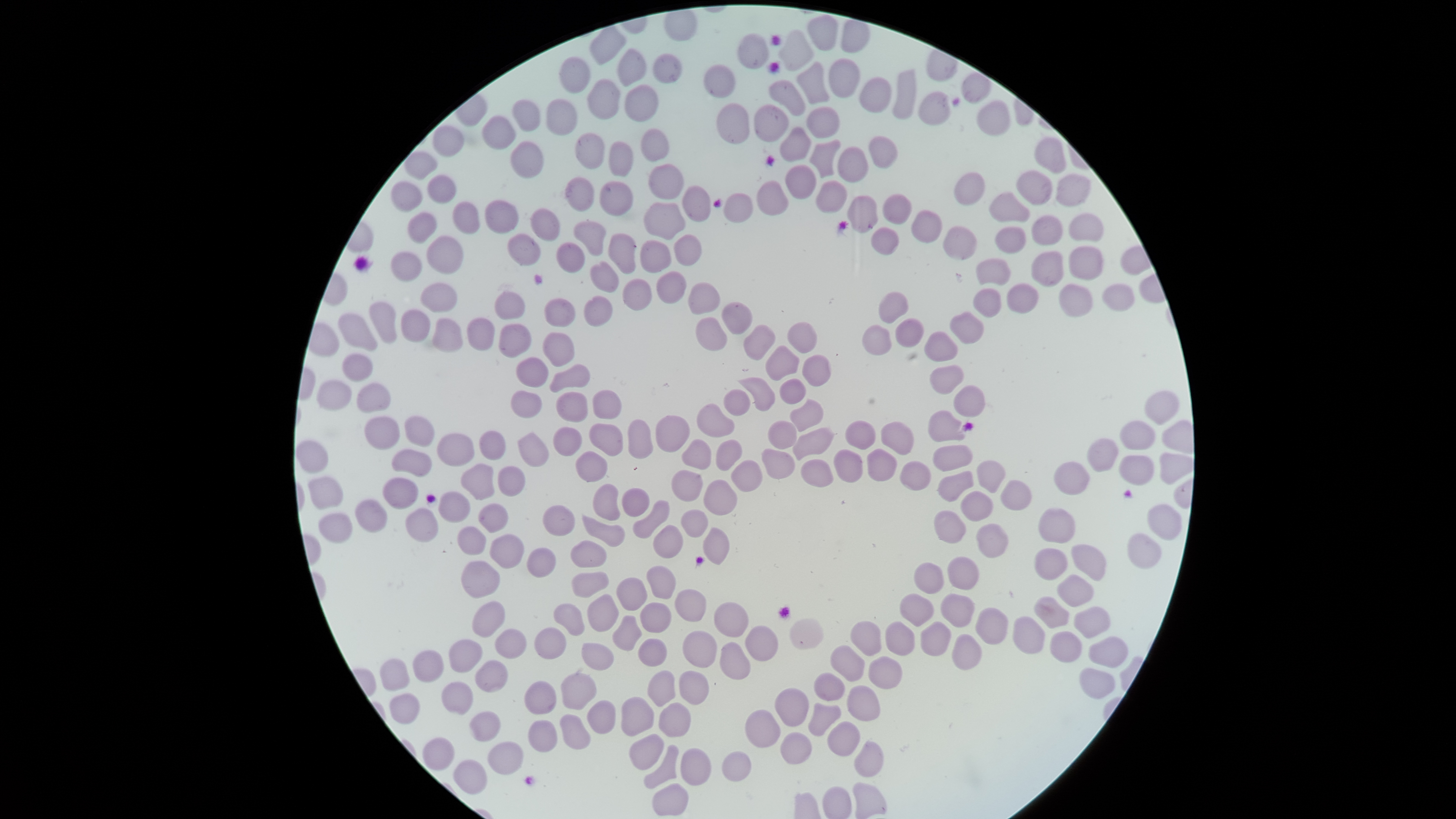
Approximate bounding boxes as (left, top, right, bottom) in pixels.
Summary:
  - Uninfected red blood cells: (807, 14, 839, 51), (842, 20, 871, 54), (589, 27, 628, 66), (777, 29, 813, 71), (738, 32, 769, 69), (618, 49, 646, 87), (651, 54, 682, 84), (560, 57, 591, 94), (828, 59, 860, 98), (799, 62, 829, 104), (704, 65, 734, 98), (893, 69, 917, 119), (859, 77, 892, 113), (770, 79, 804, 116), (588, 80, 620, 121), (625, 85, 659, 122), (919, 91, 952, 125), (512, 100, 541, 132), (545, 100, 576, 136), (978, 100, 1011, 136), (716, 104, 749, 143), (754, 104, 789, 142), (807, 106, 840, 138), (482, 116, 515, 150), (432, 126, 465, 158), (780, 127, 812, 162), (640, 128, 669, 161), (573, 133, 604, 170), (869, 135, 898, 168), (1034, 137, 1066, 173), (810, 140, 841, 178), (510, 142, 543, 178), (609, 142, 634, 178), (837, 146, 869, 182), (404, 152, 438, 179), (648, 164, 684, 200), (785, 165, 817, 199), (1015, 170, 1052, 205), (954, 173, 985, 205), (1056, 174, 1090, 206), (427, 176, 456, 204), (565, 178, 594, 212), (390, 181, 422, 213), (599, 181, 633, 216), (816, 181, 848, 213), (757, 182, 789, 215), (681, 186, 711, 222), (722, 193, 753, 223), (883, 193, 912, 224), (990, 193, 1031, 222), (485, 200, 520, 234), (452, 201, 481, 234), (643, 202, 686, 241), (529, 209, 561, 243), (911, 210, 943, 243), (406, 212, 439, 244), (1068, 213, 1104, 241), (1032, 215, 1062, 246), (573, 221, 606, 256), (942, 226, 976, 260), (996, 226, 1026, 252), (871, 227, 899, 256), (507, 233, 541, 266), (608, 234, 635, 274), (674, 235, 701, 267), (426, 236, 464, 274), (640, 240, 672, 274), (556, 242, 586, 273), (1068, 247, 1102, 280), (390, 252, 422, 282), (1031, 252, 1065, 287), (976, 258, 1012, 284), (590, 261, 619, 294), (657, 271, 687, 305), (622, 279, 652, 311), (688, 282, 720, 315), (421, 283, 457, 312), (1008, 283, 1039, 313), (1060, 284, 1093, 316), (1102, 284, 1135, 312), (973, 288, 1002, 318), (494, 292, 525, 320), (879, 293, 910, 323), (583, 295, 612, 327), (544, 298, 576, 328), (368, 302, 398, 344), (722, 302, 752, 335), (401, 310, 431, 342), (950, 311, 985, 343), (338, 313, 377, 352), (433, 318, 464, 353), (467, 318, 495, 352), (696, 318, 727, 351), (895, 318, 925, 347), (787, 322, 817, 354), (498, 324, 532, 358), (744, 324, 776, 361), (863, 325, 892, 355), (924, 332, 958, 360), (542, 333, 574, 367), (765, 345, 799, 381), (342, 353, 373, 382), (802, 356, 831, 387), (515, 357, 549, 387), (549, 365, 591, 393), (930, 366, 964, 394), (738, 378, 775, 411), (780, 379, 806, 405), (316, 380, 352, 411), (357, 383, 391, 414), (953, 384, 985, 418), (723, 390, 750, 417), (1144, 390, 1180, 425), (511, 391, 542, 419), (592, 391, 621, 420), (556, 392, 589, 422), (789, 398, 823, 432), (697, 403, 734, 438), (928, 410, 967, 442), (656, 415, 690, 453), (404, 416, 435, 447), (365, 417, 400, 450), (628, 419, 653, 459), (845, 419, 876, 450), (767, 421, 797, 450), (881, 421, 914, 455), (1120, 421, 1156, 451), (590, 423, 623, 457), (552, 427, 582, 457), (792, 428, 834, 460), (480, 431, 506, 461), (436, 433, 475, 467), (517, 433, 548, 468), (682, 438, 712, 470), (1088, 438, 1119, 472), (715, 440, 742, 471), (297, 441, 329, 474), (934, 445, 972, 471), (867, 448, 898, 482), (761, 449, 795, 481), (834, 449, 864, 482), (391, 450, 432, 478), (576, 452, 607, 482), (1119, 455, 1155, 486), (731, 460, 762, 493), (801, 460, 833, 488), (900, 460, 931, 491), (977, 460, 1006, 493), (1053, 462, 1089, 494), (460, 464, 495, 500), (497, 467, 526, 497), (671, 470, 703, 502), (937, 470, 974, 502), (309, 476, 344, 509), (383, 477, 418, 510), (1000, 479, 1033, 510), (703, 480, 738, 516), (593, 485, 620, 521), (621, 488, 650, 517), (961, 491, 994, 522), (438, 492, 470, 523), (355, 499, 387, 533), (632, 500, 670, 539), (479, 503, 508, 532), (1149, 505, 1182, 540), (543, 506, 575, 537), (1038, 508, 1076, 543), (405, 509, 439, 543), (681, 510, 708, 538), (934, 510, 966, 544), (318, 514, 352, 544), (582, 515, 625, 547), (976, 524, 1008, 559), (653, 525, 684, 559), (458, 527, 487, 554), (703, 527, 730, 565), (1128, 533, 1162, 568), (490, 535, 525, 569), (570, 540, 607, 568), (1071, 544, 1107, 581), (527, 547, 556, 577), (1034, 548, 1068, 581), (947, 557, 979, 590), (462, 561, 500, 598), (914, 562, 944, 594), (646, 565, 676, 600), (571, 571, 610, 598), (1056, 575, 1094, 607), (616, 577, 647, 611), (675, 589, 707, 622), (586, 594, 619, 632), (900, 594, 933, 627), (940, 594, 975, 627), (1034, 597, 1069, 629), (473, 601, 506, 637), (714, 602, 749, 637), (553, 603, 585, 636), (640, 603, 672, 633), (1073, 606, 1111, 639), (976, 607, 1009, 645), (612, 615, 643, 651), (1013, 616, 1045, 654), (790, 618, 823, 650), (851, 621, 881, 656), (885, 621, 914, 656), (921, 622, 951, 655), (745, 626, 778, 661), (533, 627, 567, 660), (496, 628, 527, 659), (683, 631, 717, 668), (1050, 632, 1083, 663), (951, 635, 982, 670), (1088, 637, 1129, 667), (637, 638, 668, 667), (449, 639, 483, 673), (581, 642, 615, 670), (720, 642, 751, 680), (830, 645, 865, 682), (412, 650, 444, 682), (869, 656, 903, 689), (380, 659, 410, 691), (475, 660, 508, 692), (1079, 668, 1115, 699), (646, 669, 676, 706), (679, 670, 710, 705), (560, 672, 597, 710), (813, 673, 845, 701), (524, 681, 556, 716), (443, 682, 474, 715), (847, 685, 880, 721), (775, 688, 809, 727), (389, 693, 420, 723), (621, 696, 654, 737), (587, 700, 616, 735), (658, 702, 691, 738), (807, 702, 841, 736), (745, 709, 780, 748), (468, 711, 500, 742), (559, 714, 591, 750), (527, 720, 558, 753), (827, 722, 860, 757), (781, 732, 811, 764), (629, 733, 664, 771), (424, 737, 455, 771), (854, 741, 884, 778), (488, 742, 523, 775), (643, 744, 679, 789), (680, 748, 711, 786), (721, 751, 751, 782), (453, 760, 487, 796), (652, 783, 689, 816), (853, 783, 888, 819)
  - Capture: smartphone photograph through the microscope eyepiece
  - Visible region: circular
  - Presence: no malaria parasites detected
  - Image size: 1456×819 pixels
  - Stain: Giemsa
  - Preparation: thin smear of blood
  - Field of view: single